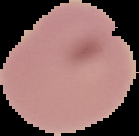

Segmented cell region on a black background. From a thin blood film. Image is 139×136 pixels. Result: no Plasmodium parasites seen.